Identify the parasite.
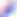
This is Toxoplasma gondii.

Summary:
  - Magnification: 400x
  - Modality: photomicrograph